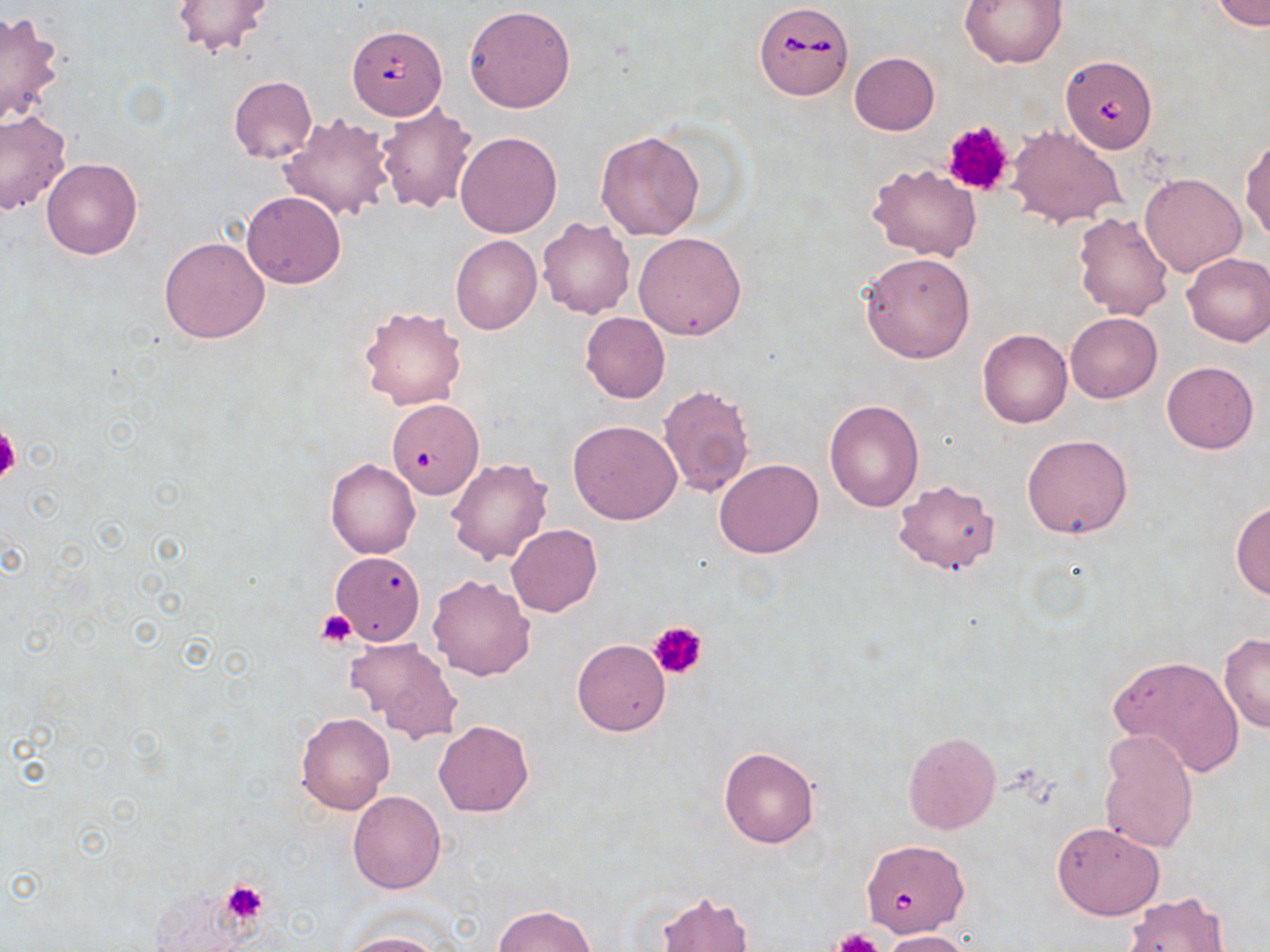

slide-level diagnosis = Babesia divergens
field of view = single
Babesia divergens-infected red blood cell locations = approximate bounding boxes as (x1,y1)-(x2,y2) corner pairs in pixels: (753,2)-(854,100), (348,24)-(447,119), (1058,56)-(1157,164), (860,840)-(970,942)
platelet locations = approximate bounding boxes as (x1,y1)-(x2,y2) corner pairs in pixels: (942,119)-(1015,195), (0,426)-(21,482), (317,610)-(358,649), (650,620)-(707,680), (222,881)-(268,924), (832,929)-(883,952)
image size = 1270×952 pixels
stain = May-Grünwald-Giemsa
modality = light microscopy
preparation = thin blood smear
uninfected red blood cell locations = approximate bounding boxes as (x1,y1)-(x2,y2) corner pairs in pixels: (959,0)-(1066,69), (1213,0)-(1269,29), (168,1)-(278,61), (463,5)-(575,113), (0,10)-(65,129), (849,51)-(939,134), (228,76)-(318,164), (376,103)-(478,214), (0,110)-(72,215), (279,113)-(396,221), (1008,125)-(1126,228), (595,130)-(706,241), (455,131)-(561,239), (1241,138)-(1270,244), (41,158)-(142,259), (869,162)-(980,260), (1140,173)-(1246,276), (1082,179)-(1208,296), (242,191)-(346,288), (1072,212)-(1173,319), (537,216)-(636,319), (633,231)-(747,340), (450,235)-(542,334), (159,236)-(270,344), (860,251)-(976,363), (1181,251)-(1270,347), (359,306)-(466,411), (581,312)-(670,403), (1066,312)-(1161,404), (978,329)-(1073,428), (1162,361)-(1259,454), (658,384)-(755,497), (824,398)-(925,512), (385,400)-(484,501), (568,420)-(682,525), (1022,434)-(1133,539), (325,458)-(421,560), (447,458)-(554,565), (714,458)-(824,559), (894,480)-(999,574), (1230,501)-(1270,599), (506,525)-(602,616), (330,551)-(425,646), (427,573)-(536,681), (1218,634)-(1270,733), (346,637)-(464,739), (572,638)-(670,736), (1110,654)-(1245,776), (296,713)-(394,814), (433,719)-(534,817), (902,732)-(1000,834), (1098,732)-(1197,853), (719,747)-(818,848), (347,790)-(446,894), (1051,821)-(1165,920), (654,890)-(755,952), (1122,892)-(1230,951), (493,904)-(597,952), (882,929)-(975,952), (337,931)-(447,952)
magnification = 1000x